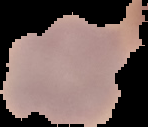

malaria status = uninfected
preparation = thin blood smear
image type = segmented cell region with the area outside set to black
image size = 148×127 pixels